Outline each blood parasite and name the species.
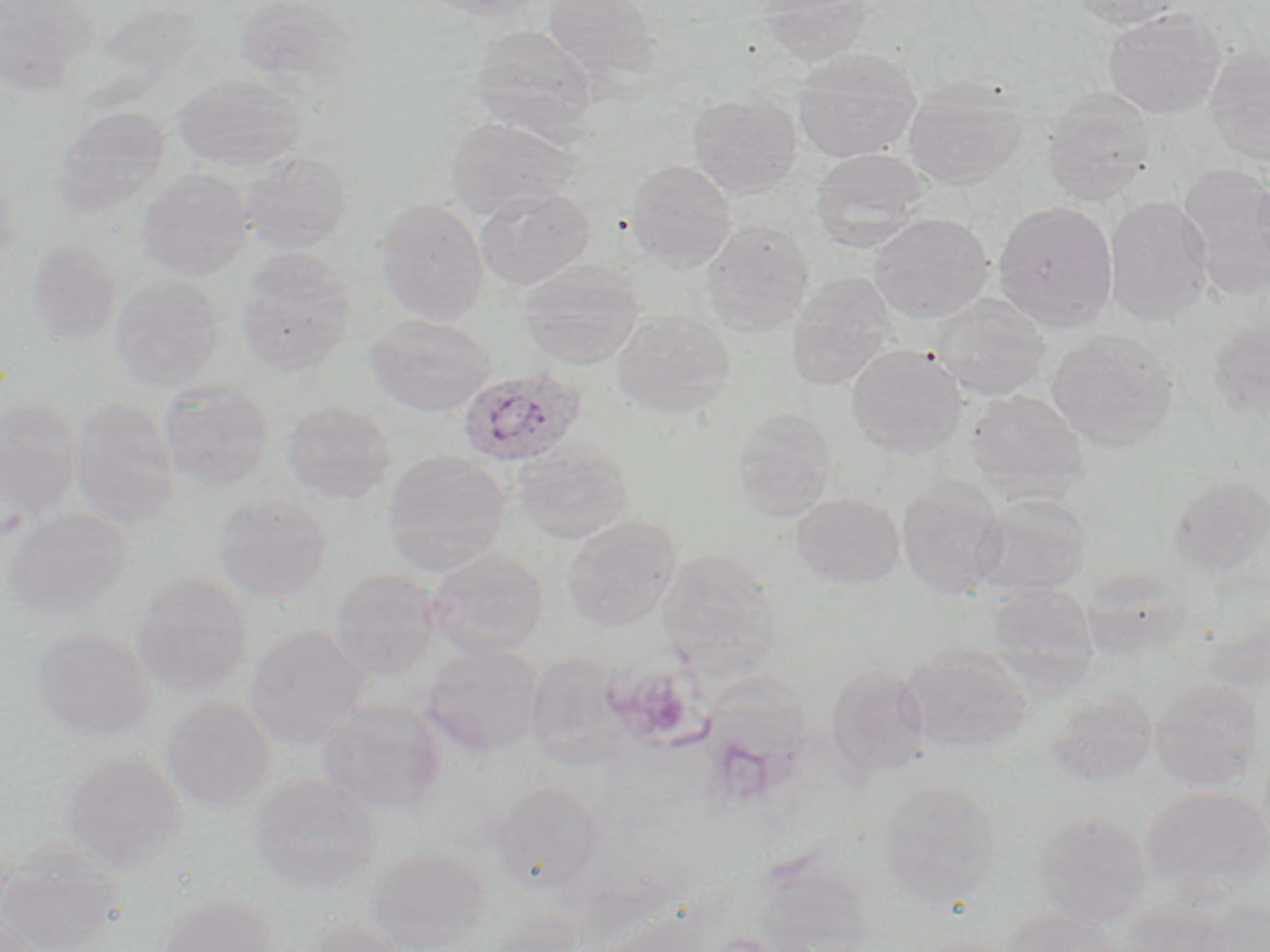
Approximate bounding boxes as named x1/y1/x2/y2 corners in pixels.
Plasmodium ovale-infected red blood cells: (x1=457, y1=366, x2=587, y2=468).
No Plasmodium falciparum, Plasmodium malariae, Plasmodium vivax, Babesia divergens, or Trypanosoma brucei observed.

Platelet locations: (x1=603, y1=667, x2=702, y2=745). Uninfected red blood cell locations: (x1=233, y1=0, x2=360, y2=96), (x1=422, y1=0, x2=545, y2=18), (x1=541, y1=0, x2=663, y2=84), (x1=757, y1=0, x2=874, y2=68), (x1=1072, y1=0, x2=1186, y2=29), (x1=0, y1=1, x2=99, y2=93), (x1=1102, y1=8, x2=1225, y2=119), (x1=470, y1=24, x2=599, y2=140), (x1=1205, y1=45, x2=1270, y2=168), (x1=792, y1=47, x2=921, y2=163), (x1=173, y1=73, x2=307, y2=171), (x1=903, y1=77, x2=1027, y2=189), (x1=1042, y1=87, x2=1157, y2=204), (x1=687, y1=92, x2=802, y2=197), (x1=52, y1=105, x2=171, y2=219), (x1=444, y1=114, x2=583, y2=221), (x1=239, y1=147, x2=353, y2=254), (x1=810, y1=148, x2=930, y2=253), (x1=625, y1=159, x2=737, y2=271), (x1=1177, y1=164, x2=1270, y2=300), (x1=136, y1=168, x2=253, y2=281), (x1=1252, y1=172, x2=1270, y2=279), (x1=474, y1=187, x2=595, y2=291), (x1=1104, y1=196, x2=1214, y2=325), (x1=374, y1=198, x2=488, y2=325), (x1=992, y1=201, x2=1118, y2=331), (x1=869, y1=213, x2=994, y2=322), (x1=701, y1=219, x2=815, y2=333), (x1=25, y1=238, x2=122, y2=346), (x1=236, y1=247, x2=355, y2=375), (x1=519, y1=259, x2=644, y2=369), (x1=111, y1=273, x2=226, y2=389), (x1=785, y1=274, x2=897, y2=392), (x1=928, y1=293, x2=1051, y2=401), (x1=612, y1=309, x2=735, y2=419), (x1=364, y1=314, x2=495, y2=417), (x1=1207, y1=318, x2=1270, y2=421), (x1=1047, y1=329, x2=1179, y2=452), (x1=845, y1=343, x2=967, y2=458), (x1=157, y1=380, x2=273, y2=491), (x1=966, y1=389, x2=1088, y2=498), (x1=0, y1=398, x2=83, y2=529), (x1=70, y1=399, x2=180, y2=527), (x1=282, y1=401, x2=397, y2=504), (x1=731, y1=409, x2=837, y2=521), (x1=511, y1=442, x2=635, y2=544), (x1=381, y1=450, x2=514, y2=575), (x1=1166, y1=473, x2=1270, y2=580), (x1=897, y1=476, x2=1008, y2=600), (x1=972, y1=492, x2=1092, y2=596), (x1=212, y1=493, x2=332, y2=602), (x1=792, y1=493, x2=904, y2=589), (x1=2, y1=508, x2=133, y2=618), (x1=561, y1=515, x2=681, y2=632), (x1=425, y1=548, x2=549, y2=658), (x1=656, y1=548, x2=780, y2=666), (x1=328, y1=568, x2=442, y2=679), (x1=131, y1=572, x2=252, y2=696), (x1=986, y1=582, x2=1099, y2=687), (x1=245, y1=626, x2=371, y2=746), (x1=30, y1=628, x2=154, y2=741), (x1=900, y1=643, x2=1034, y2=756), (x1=420, y1=644, x2=545, y2=757), (x1=526, y1=653, x2=628, y2=765), (x1=826, y1=662, x2=930, y2=778), (x1=712, y1=676, x2=813, y2=803), (x1=1148, y1=677, x2=1264, y2=792), (x1=1046, y1=689, x2=1159, y2=786), (x1=160, y1=698, x2=275, y2=811), (x1=315, y1=699, x2=445, y2=814), (x1=60, y1=752, x2=188, y2=870), (x1=248, y1=774, x2=381, y2=891), (x1=878, y1=780, x2=1003, y2=900), (x1=491, y1=782, x2=604, y2=894), (x1=1141, y1=785, x2=1270, y2=896), (x1=1031, y1=810, x2=1153, y2=927), (x1=0, y1=842, x2=124, y2=952), (x1=366, y1=847, x2=494, y2=951), (x1=158, y1=893, x2=277, y2=952), (x1=1115, y1=900, x2=1241, y2=952), (x1=999, y1=908, x2=1121, y2=952), (x1=1, y1=911, x2=47, y2=951), (x1=587, y1=913, x2=714, y2=952), (x1=297, y1=918, x2=406, y2=952). Slide-level diagnosis: Plasmodium ovale. May-Grünwald-Giemsa stain. Thin blood smear. Image is 1270×952 pixels. Captured at 1000x magnification. One field of a larger specimen. Optical microscopy.